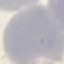

Malaria status: uninfected. Giemsa-stained preparation. Cell patch, automatically extracted from a larger field of view and resized to 64 × 64 pixels. Photographed with a smartphone camera at the microscope eyepiece. Thin blood film.